Name the cell type shown.
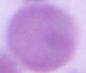
This is an erythrocyte.

Photomicrograph. 1000x magnification.